Assess this cell for malaria.
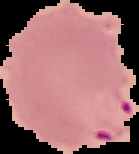

It is parasitized.

Segmented cell region on a black background. From a thin blood film. Image is 139×154 pixels.